Report the malaria status of this cell.
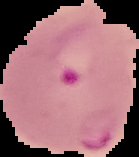
It is parasitized.

Image is 139×157 pixels. Segmented cell region on a black background. From a thin blood film.